Locate and identify every blood parasite.
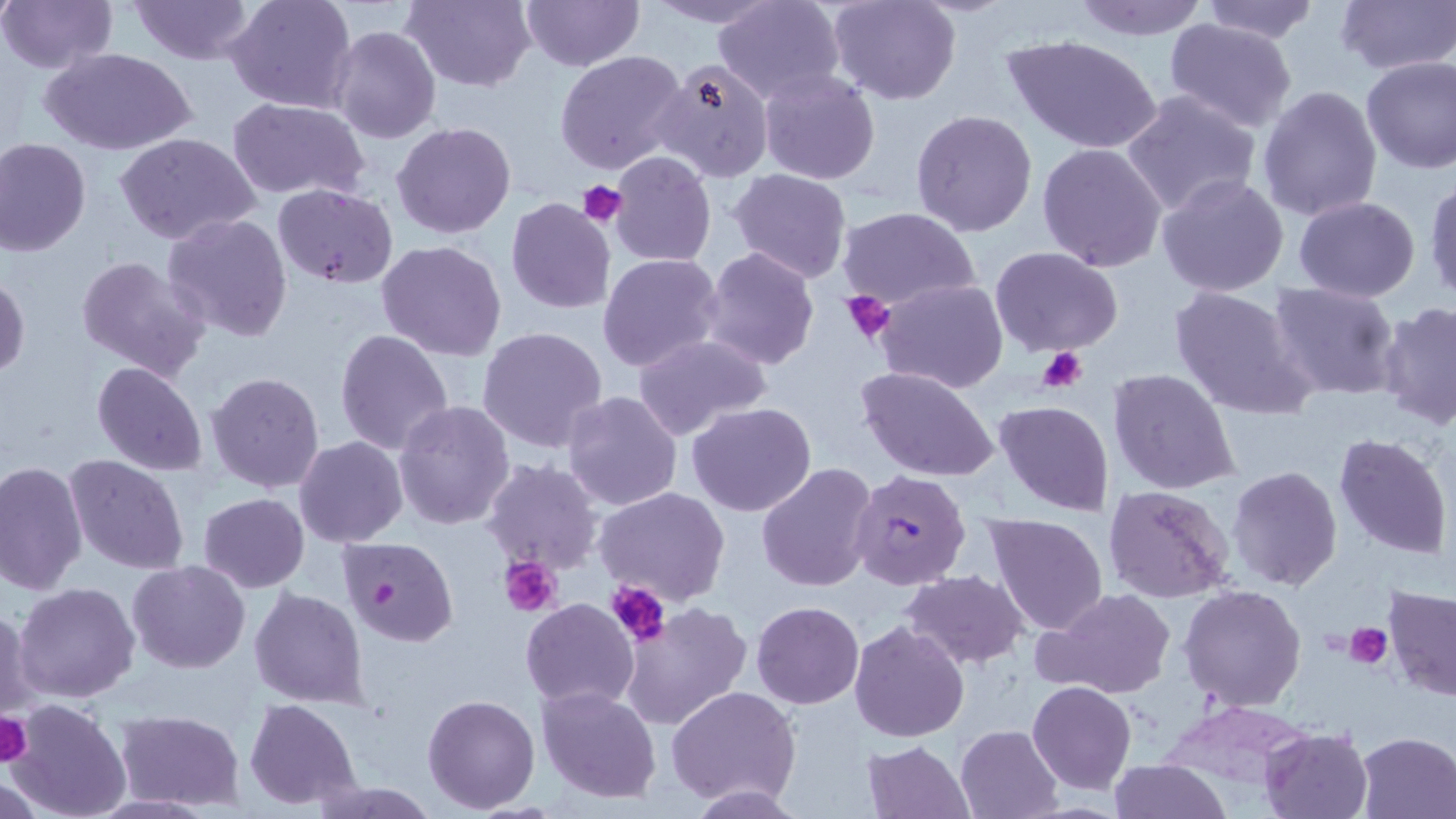

Approximate bounding boxes as (x1, y1, x2, y2) in pixels.
Plasmodium falciparum-infected red blood cells: (847, 470, 972, 590), (335, 534, 460, 648).
No Plasmodium ovale, Plasmodium malariae, Plasmodium vivax, Babesia divergens, or Trypanosoma brucei observed.

Platelet locations: (580, 182, 625, 228), (840, 291, 896, 344), (1038, 347, 1088, 393), (502, 557, 562, 617), (606, 580, 671, 645), (1346, 623, 1391, 668), (0, 711, 32, 765). Uninfected red blood cell locations: (1, 0, 118, 75), (129, 0, 257, 65), (225, 0, 357, 114), (401, 0, 535, 93), (520, 0, 643, 71), (645, 0, 777, 27), (827, 0, 963, 104), (1070, 0, 1209, 41), (1196, 0, 1320, 44), (1333, 0, 1456, 78), (714, 1, 845, 103), (728, 6, 947, 130), (1163, 18, 1298, 133), (329, 26, 441, 143), (1003, 33, 1162, 154), (42, 47, 196, 156), (555, 49, 688, 176), (1360, 56, 1456, 175), (649, 57, 774, 183), (758, 70, 883, 185), (1256, 85, 1384, 222), (1121, 89, 1262, 218), (227, 98, 373, 199), (912, 108, 1038, 237), (392, 121, 517, 240), (113, 132, 262, 245), (0, 137, 92, 256), (1037, 141, 1167, 272), (609, 152, 716, 266), (730, 168, 852, 283), (1157, 171, 1290, 297), (1424, 179, 1456, 304), (272, 182, 398, 288), (505, 197, 616, 314), (1294, 197, 1421, 302), (836, 206, 981, 312), (161, 212, 294, 343), (377, 241, 508, 362), (699, 246, 819, 371), (990, 246, 1123, 357), (597, 252, 724, 374), (75, 256, 213, 383), (0, 271, 29, 380), (875, 278, 1008, 393), (1267, 281, 1401, 399), (1168, 284, 1317, 421), (1376, 303, 1456, 430), (476, 325, 608, 455), (334, 330, 454, 458), (633, 334, 773, 440), (92, 361, 209, 477), (855, 364, 1000, 483), (1107, 369, 1239, 497), (205, 372, 325, 493), (561, 390, 684, 511), (393, 400, 516, 529), (687, 401, 817, 517), (993, 401, 1113, 517), (1332, 432, 1453, 559), (294, 436, 408, 548), (64, 453, 191, 575), (480, 458, 602, 576), (0, 461, 88, 593), (756, 461, 879, 593), (1226, 466, 1344, 591), (1104, 486, 1235, 604), (594, 487, 732, 607), (198, 493, 309, 592), (985, 513, 1109, 636), (127, 560, 252, 673), (902, 570, 1030, 669), (13, 581, 139, 704), (1179, 585, 1307, 712), (1383, 585, 1456, 702), (249, 587, 372, 709), (1038, 587, 1176, 700), (520, 599, 638, 711), (617, 601, 752, 730), (752, 601, 864, 709), (0, 605, 36, 722), (848, 621, 969, 742), (1027, 681, 1136, 794), (536, 684, 662, 804), (666, 685, 803, 807), (422, 693, 540, 811), (244, 698, 361, 807), (5, 700, 133, 819), (115, 709, 243, 810), (955, 724, 1063, 818), (1260, 727, 1373, 818), (1355, 731, 1456, 817), (862, 740, 975, 819), (1109, 758, 1231, 818), (306, 781, 439, 817), (685, 784, 809, 816). Slide-level diagnosis: Plasmodium falciparum. May-Grünwald-Giemsa stain. Optical microscopy. One field of a larger specimen. Captured at 1000x magnification. Thin blood film. Image is 1456×819 pixels.